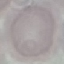
Summary:
  - Malaria status: uninfected
  - Image type: cell patch, automatically extracted from a larger field of view and resized to 64 × 64 pixels
  - Stain: Giemsa
  - Capture: smartphone camera at the microscope eyepiece
  - Preparation: thin blood film